Report the malaria status of this cell.
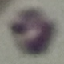
Uninfected.

Summary:
  - Preparation: thin blood smear
  - Stain: Giemsa
  - Capture: smartphone through the microscope eyepiece
  - Image type: automatically extracted cell patch, resized to 64 × 64 pixels